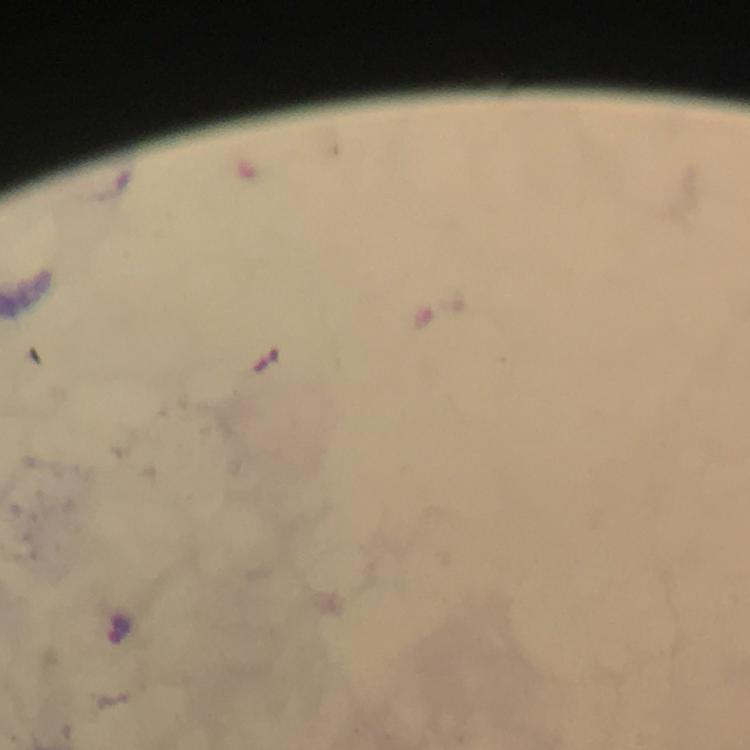
Approximate centers as {x, y} in pixels.
Summary:
  - Malaria parasite locations: {122, 630}
  - Stain: Giemsa
  - Preparation: thick blood film
  - Immersion oil: applied
  - Cropped from: a single field of view
  - Context: from a diagnostic examination for malaria
  - Capture: smartphone camera through the microscope
  - Image size: 750×750 pixels
  - Magnification: 100x